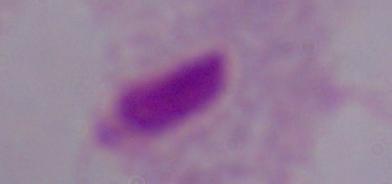
modality: photomicrograph
magnification: 1000x
identification: trichomonad